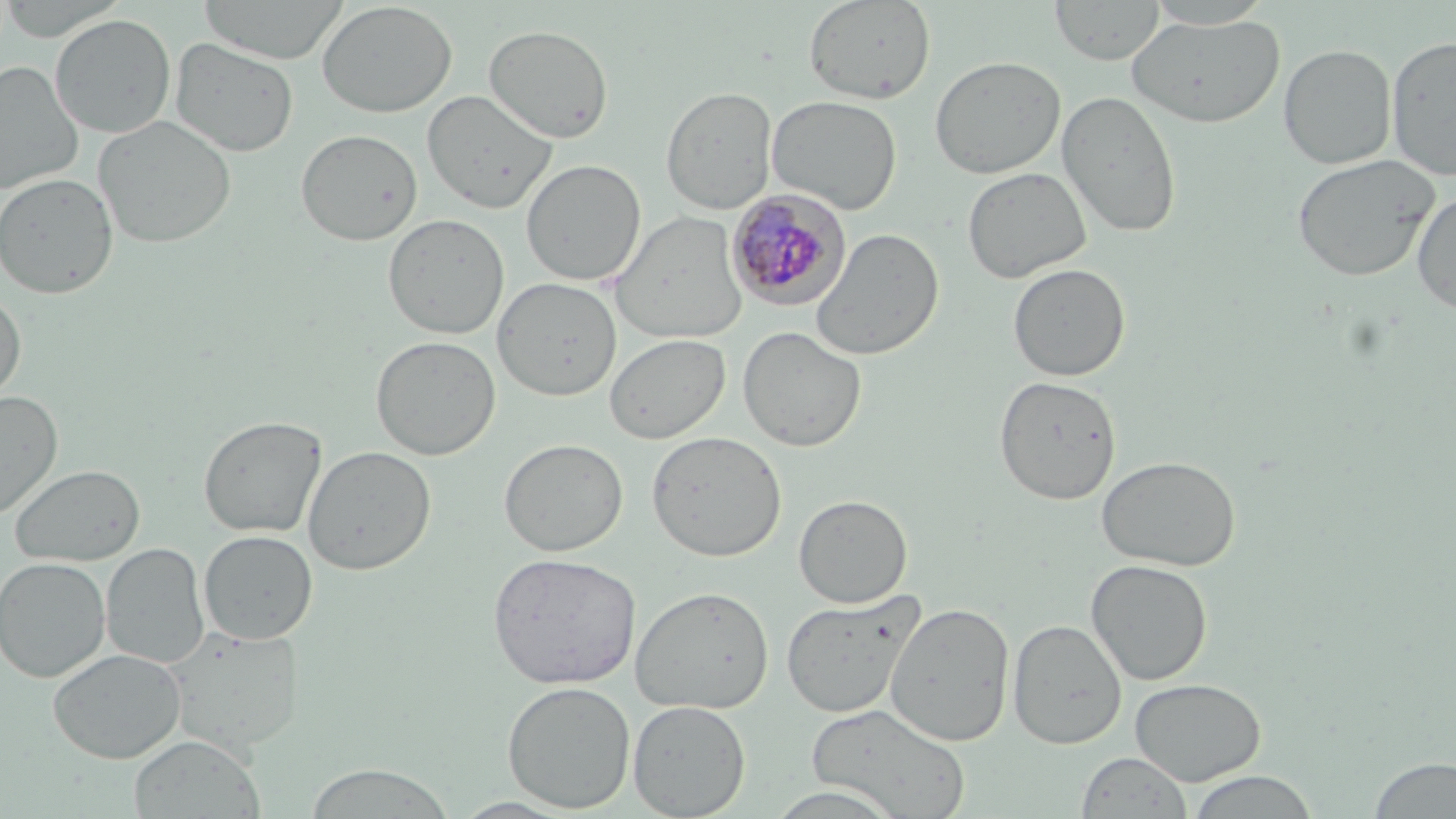

Summary:
  - Coordinate format: approximate bounding boxes as (x1,y1)-(x2,y2) corner pairs in pixels
  - Plasmodium malariae-infected red blood cell locations: (726,189)-(851,310)
  - Uninfected red blood cell locations: (0,0)-(130,40), (197,0)-(350,64), (803,0)-(936,104), (1050,0)-(1165,65), (1144,0)-(1276,29), (316,1)-(457,118), (50,14)-(177,138), (1126,14)-(1285,129), (483,24)-(614,143), (1386,34)-(1456,182), (170,38)-(299,157), (1278,44)-(1397,169), (929,55)-(1066,178), (0,61)-(83,195), (661,86)-(778,214), (1056,89)-(1182,238), (422,90)-(557,214), (767,94)-(902,214), (94,115)-(237,248), (295,129)-(423,246), (1291,154)-(1440,282), (521,159)-(646,286), (962,166)-(1092,283), (0,172)-(118,298), (1412,191)-(1456,315), (609,210)-(749,345), (383,213)-(510,339), (810,229)-(944,360), (1008,263)-(1131,381), (492,277)-(622,401), (0,289)-(26,406), (737,326)-(867,452), (604,333)-(730,444), (370,335)-(501,460), (994,375)-(1122,505), (0,390)-(63,520), (198,415)-(327,538), (646,431)-(786,562), (498,438)-(628,557), (302,445)-(437,576), (1096,455)-(1242,572), (9,464)-(145,566), (793,494)-(913,608), (199,530)-(317,644), (101,543)-(209,669), (487,551)-(642,689), (0,557)-(111,682), (1085,559)-(1213,686), (630,585)-(775,714), (779,590)-(925,719), (884,601)-(1015,747), (1008,618)-(1127,748), (163,626)-(305,754), (48,648)-(186,763), (1130,677)-(1266,785), (501,680)-(636,813), (627,700)-(751,817), (806,703)-(970,818), (129,735)-(264,819), (1076,751)-(1192,818), (1367,756)-(1456,817), (302,764)-(457,818), (1183,771)-(1321,818), (761,785)-(907,819)
  - Slide-level diagnosis: Plasmodium malariae
  - Field of view: one of a larger specimen
  - Preparation: thin blood smear
  - Magnification: 1000x
  - Image size: 1456×819 pixels
  - Modality: light microscopy
  - Stain: May-Grünwald-Giemsa